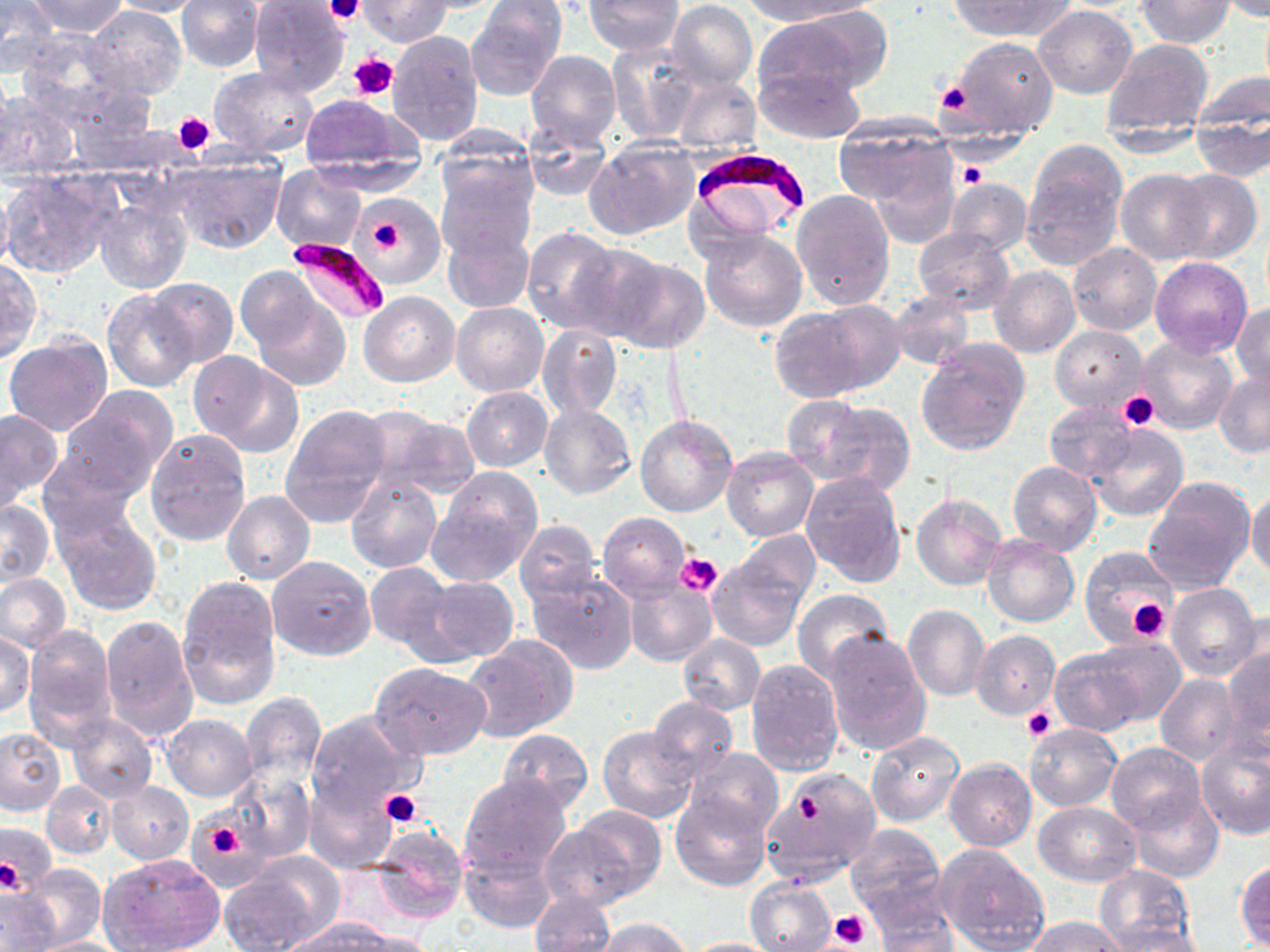
Summary:
  - Coordinate format: approximate bounding boxes as [x1, y1, x2, y2] in pixels
  - Uninfected red blood cell locations: [0, 0, 61, 74], [29, 0, 128, 37], [108, 0, 205, 17], [582, 0, 683, 56], [740, 0, 864, 26], [948, 0, 1072, 40], [1136, 0, 1234, 48], [1218, 0, 1270, 22], [22, 1, 129, 76], [175, 1, 265, 73], [248, 1, 352, 95], [360, 1, 451, 47], [668, 1, 757, 90], [468, 3, 565, 99], [85, 4, 187, 98], [1034, 6, 1137, 99], [1259, 6, 1270, 93], [752, 11, 880, 106], [14, 28, 132, 124], [387, 30, 483, 146], [1101, 37, 1213, 142], [944, 38, 1058, 144], [607, 42, 704, 145], [525, 50, 622, 150], [0, 61, 15, 172], [755, 64, 864, 141], [208, 67, 320, 160], [1190, 70, 1269, 142], [672, 74, 760, 155], [0, 89, 82, 180], [295, 95, 423, 188], [833, 117, 953, 213], [1192, 117, 1269, 182], [433, 121, 539, 213], [521, 122, 612, 200], [586, 139, 699, 238], [1021, 148, 1125, 271], [171, 153, 287, 255], [434, 157, 537, 263], [272, 164, 367, 252], [867, 165, 958, 250], [1, 168, 120, 278], [1116, 169, 1211, 264], [1167, 169, 1262, 264], [943, 177, 1031, 256], [792, 189, 896, 310], [360, 193, 444, 282], [94, 195, 193, 295], [442, 225, 534, 314], [521, 226, 623, 335], [913, 228, 1015, 315], [699, 229, 807, 332], [563, 242, 674, 341], [1067, 243, 1162, 337], [602, 254, 711, 354], [1150, 256, 1253, 358], [0, 259, 41, 363], [989, 265, 1081, 359], [146, 277, 239, 367], [242, 279, 352, 390], [103, 289, 200, 391], [358, 291, 459, 387], [887, 291, 974, 371], [451, 302, 549, 398], [769, 302, 899, 403], [1233, 304, 1270, 391], [537, 324, 622, 421], [1051, 324, 1147, 414], [3, 335, 112, 436], [1135, 337, 1237, 435], [916, 340, 1029, 457], [188, 351, 303, 456], [1213, 371, 1270, 457], [463, 386, 552, 471], [59, 389, 177, 497], [783, 396, 875, 478], [806, 400, 916, 496], [538, 403, 636, 499], [1044, 403, 1137, 483], [281, 406, 391, 523], [0, 407, 63, 509], [359, 409, 480, 499], [636, 415, 737, 517], [1088, 423, 1189, 521], [145, 429, 251, 547], [1101, 441, 1214, 565], [722, 449, 819, 541], [38, 450, 139, 541], [1008, 461, 1102, 555], [426, 468, 542, 588], [345, 471, 441, 573], [801, 472, 906, 590], [1142, 479, 1256, 594], [1247, 488, 1270, 579], [222, 491, 315, 584], [911, 494, 1006, 592], [0, 499, 55, 585], [51, 502, 162, 614], [598, 513, 689, 602], [515, 519, 604, 610], [732, 531, 821, 610], [982, 533, 1079, 628], [1079, 545, 1182, 651], [707, 554, 810, 653], [268, 556, 376, 661], [363, 560, 458, 658], [527, 568, 638, 673], [0, 573, 72, 654], [177, 575, 281, 706], [424, 577, 519, 663], [624, 580, 716, 666], [1165, 583, 1262, 682], [790, 589, 895, 683], [903, 605, 990, 702], [99, 616, 199, 740], [22, 624, 117, 745], [824, 628, 932, 755], [971, 630, 1062, 721], [1, 631, 35, 718], [678, 634, 766, 715], [1086, 637, 1185, 725], [461, 639, 575, 743], [1222, 644, 1270, 750], [1048, 648, 1147, 736], [745, 658, 845, 776], [371, 661, 492, 760], [1155, 673, 1243, 766], [239, 692, 327, 787], [646, 696, 738, 781], [306, 710, 424, 819], [67, 712, 158, 803], [162, 714, 258, 800], [1026, 722, 1122, 811], [597, 726, 697, 822], [0, 727, 68, 817], [498, 728, 593, 813], [865, 728, 965, 826], [1197, 740, 1270, 840], [1105, 742, 1205, 835], [684, 747, 783, 838], [944, 757, 1036, 851], [224, 767, 314, 862], [759, 767, 883, 888], [457, 775, 574, 882], [43, 780, 117, 859], [107, 781, 194, 864], [303, 784, 393, 874], [669, 789, 771, 891], [1122, 789, 1225, 884], [1034, 802, 1141, 885], [560, 804, 667, 906], [0, 821, 57, 896], [844, 823, 945, 920], [369, 825, 470, 925], [936, 846, 1048, 952], [460, 852, 555, 933], [97, 854, 226, 952], [1234, 859, 1270, 950], [218, 861, 334, 952], [16, 865, 107, 949], [1093, 865, 1195, 949], [744, 876, 837, 951], [866, 887, 959, 952], [0, 889, 59, 951], [528, 892, 615, 952], [287, 917, 396, 950], [1025, 917, 1127, 952], [593, 918, 692, 952], [1098, 925, 1210, 951], [337, 929, 439, 952], [24, 935, 129, 952], [678, 937, 790, 951]
  - Plasmodium falciparum-infected red blood cell locations: [691, 145, 811, 220], [287, 236, 391, 324]
  - Platelet locations: [325, 0, 364, 25], [349, 51, 400, 101], [937, 82, 974, 114], [171, 110, 216, 155], [956, 163, 985, 190], [362, 207, 416, 265], [1118, 393, 1157, 430], [676, 552, 721, 595], [1103, 577, 1171, 644], [1128, 597, 1171, 642], [1023, 706, 1057, 742], [379, 788, 424, 828], [798, 792, 822, 821], [206, 819, 243, 858], [0, 858, 21, 893], [829, 907, 872, 947]
  - Slide-level diagnosis: Plasmodium falciparum
  - Image size: 1270×952 pixels
  - Preparation: thin blood film
  - Modality: optical microscopy
  - Stain: May-Grünwald-Giemsa
  - Field of view: single
  - Magnification: 1000x